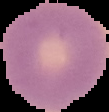
image size = 109×112 pixels
image type = segmented cell region with the area outside set to black
preparation = thin blood film
result = negative for malaria parasites